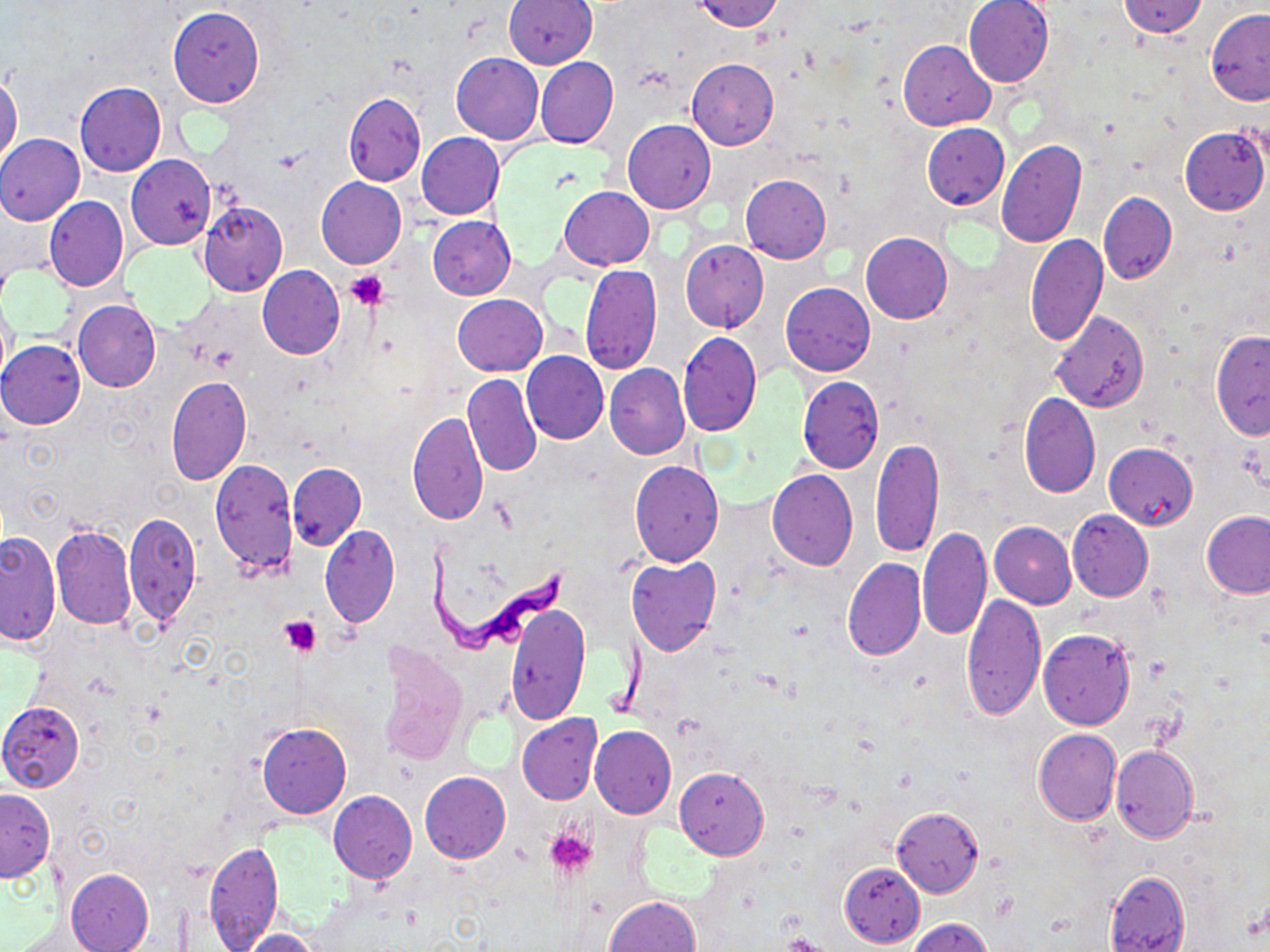
Summary:
  - Coordinate format: approximate bounding boxes as [x1, y1, x2, y2] in pixels
  - Platelet locations: [345, 271, 390, 311], [281, 614, 322, 657], [545, 828, 597, 880], [781, 934, 831, 952]
  - Uninfected red blood cell locations: [689, 0, 785, 31], [962, 0, 1055, 87], [1118, 0, 1207, 38], [504, 1, 596, 70], [168, 7, 265, 108], [1206, 9, 1270, 104], [899, 40, 995, 130], [451, 53, 543, 144], [536, 57, 617, 148], [688, 59, 778, 150], [0, 75, 22, 167], [75, 82, 166, 177], [343, 93, 426, 185], [623, 119, 716, 213], [922, 124, 1008, 209], [1179, 127, 1269, 215], [416, 132, 504, 219], [0, 134, 85, 225], [996, 141, 1086, 247], [127, 154, 215, 249], [740, 173, 831, 263], [316, 176, 406, 269], [559, 186, 654, 269], [1098, 191, 1176, 285], [43, 196, 128, 292], [198, 202, 287, 297], [428, 216, 516, 300], [861, 233, 952, 324], [1025, 234, 1107, 346], [680, 239, 768, 332], [581, 264, 662, 374], [257, 266, 345, 359], [781, 283, 875, 375], [1, 293, 16, 384], [453, 293, 547, 375], [73, 299, 160, 392], [1050, 310, 1149, 412], [1211, 330, 1270, 439], [677, 332, 761, 437], [0, 340, 86, 429], [522, 351, 608, 444], [605, 363, 689, 459], [462, 373, 541, 477], [166, 376, 251, 485], [797, 376, 884, 473], [1018, 392, 1099, 498], [409, 412, 489, 526], [871, 437, 943, 560], [1104, 441, 1198, 530], [210, 458, 298, 576], [629, 460, 724, 566], [287, 462, 366, 550], [767, 469, 858, 571], [1067, 510, 1153, 600], [125, 511, 200, 626], [1203, 511, 1270, 599], [989, 522, 1077, 608], [49, 523, 135, 629], [320, 524, 399, 628], [918, 526, 990, 640], [0, 531, 61, 645], [626, 556, 721, 657], [842, 558, 925, 661], [963, 594, 1046, 720], [507, 605, 589, 723], [1038, 629, 1135, 729], [377, 644, 468, 766], [1, 701, 85, 791], [516, 713, 602, 805], [257, 723, 351, 818], [589, 725, 676, 819], [1034, 728, 1120, 824], [1111, 745, 1198, 843], [675, 767, 767, 860], [419, 772, 511, 863], [0, 789, 54, 880], [328, 790, 417, 883], [891, 807, 984, 896], [204, 841, 284, 950], [839, 861, 925, 949], [67, 868, 154, 952], [1105, 871, 1189, 952], [602, 896, 700, 952], [909, 918, 992, 952], [238, 929, 323, 952]
  - Trypanosoma brucei locations: [422, 544, 570, 657]
  - Slide-level diagnosis: Trypanosoma brucei
  - Field of view: one of a larger specimen
  - Image size: 1270×952 pixels
  - Magnification: 1000x
  - Preparation: thin blood smear
  - Stain: May-Grünwald-Giemsa
  - Modality: optical microscopy